Point out each Plasmodium parasite.
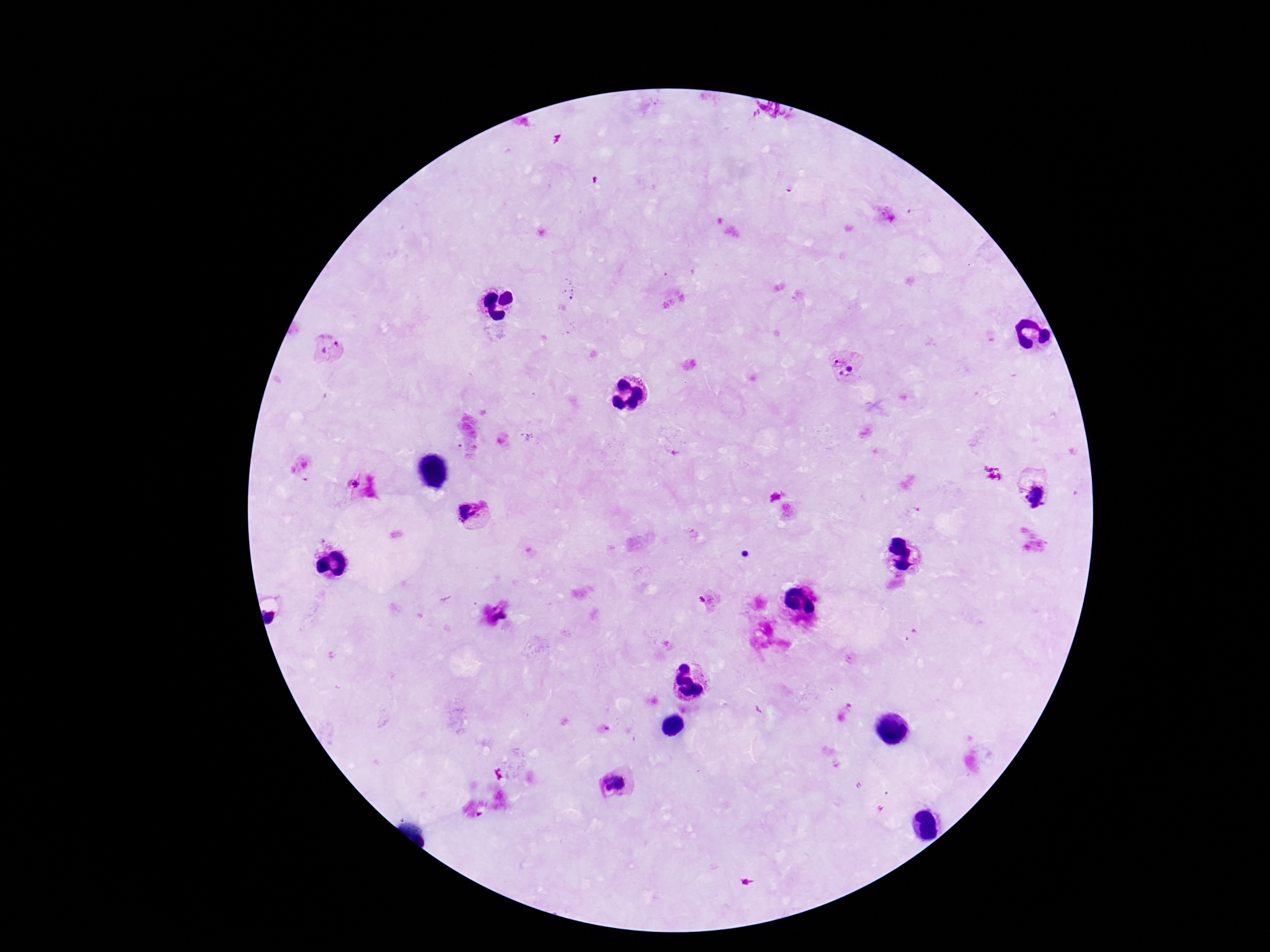
Approximate centers as [x, y] in pixels.
Plasmodium parasites: [329, 347], [838, 359], [850, 369], [841, 373], [352, 484], [1035, 496], [470, 513], [704, 601], [272, 614], [501, 617], [614, 784].

Summary:
  - Capture: smartphone camera through the microscope eyepiece
  - Patient malaria status: infected
  - Stain: Giemsa
  - Field of view: single
  - Image size: 1270×952 pixels
  - Magnification: 100x
  - Preparation: thick blood smear